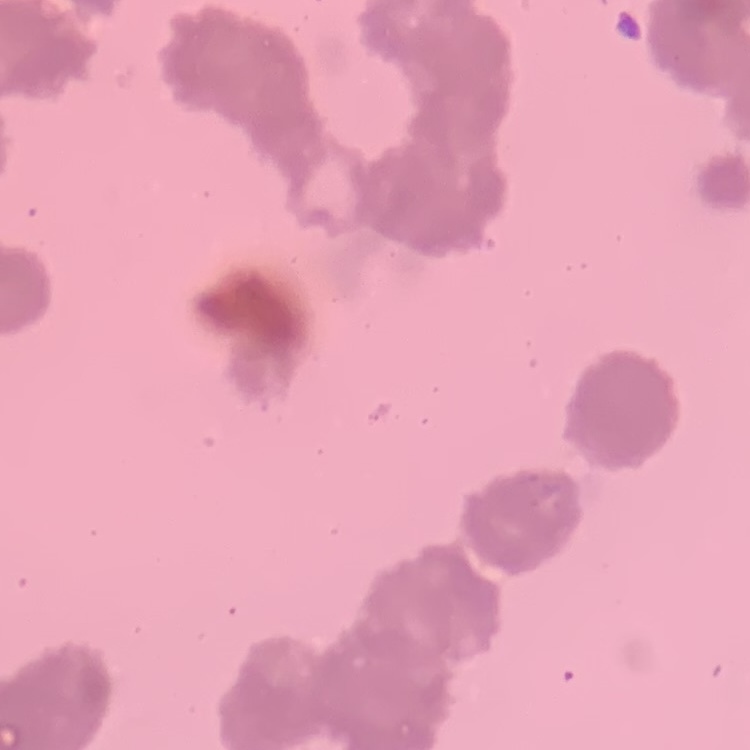
{
  "red_blood_cell_morphology": "rouleaux formation",
  "preparation": "thin blood smear",
  "stain": "Field's or Giemsa",
  "image_type": "square crop of a larger photomicrograph"
}